Give the position of every malaria parasite and every leukocyte.
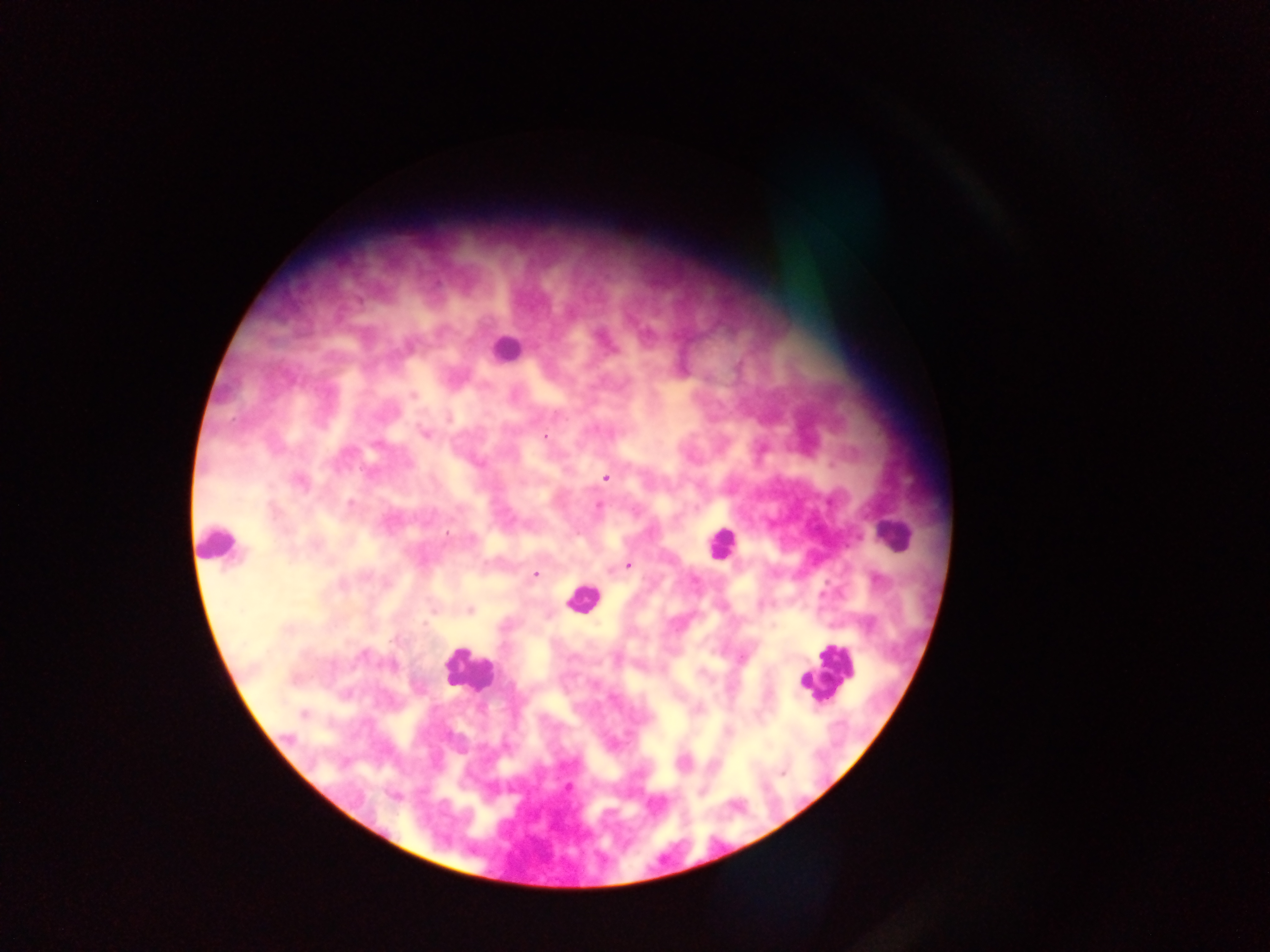

Approximate centers as x y in pixels.
Malaria parasites: 646 334; 413 396; 448 418; 425 433; 545 436; 377 446; 606 478; 300 482; 350 503; 599 506; 446 534; 629 565; 535 575; 695 581; 470 610; 425 624; 360 656; 392 665; 303 714; 287 737; 568 787; 394 797.
Leukocytes: 505 348; 891 534; 217 543; 720 544; 581 599; 468 670; 826 671.

Summary:
  - Image size: 1270×952 pixels
  - Capture: mobile-phone photograph through a microscope
  - Preparation: thick blood film
  - Country: Ghana
  - Field of view: single